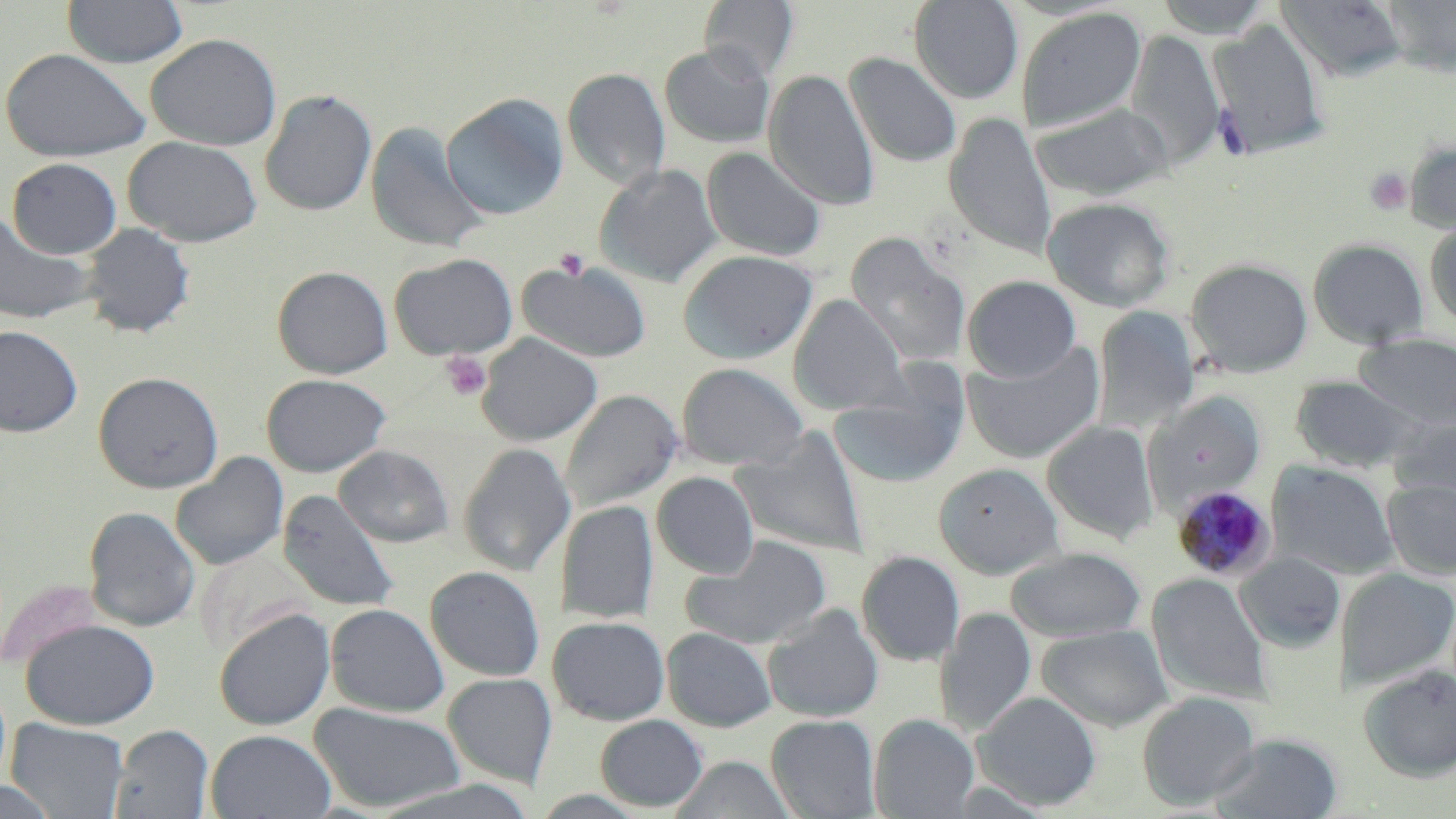
{
  "slide_level_diagnosis": "Plasmodium malariae",
  "modality": "optical microscopy",
  "uninfected_red_blood_cell_locations": "approximate bounding boxes as named x1/y1/x2/y2 corners in pixels: (x1=62, y1=0, x2=188, y2=68), (x1=699, y1=0, x2=798, y2=82), (x1=909, y1=0, x2=1024, y2=103), (x1=1153, y1=0, x2=1276, y2=38), (x1=1276, y1=0, x2=1408, y2=82), (x1=1380, y1=1, x2=1456, y2=77), (x1=1015, y1=6, x2=1147, y2=134), (x1=1209, y1=18, x2=1330, y2=158), (x1=1125, y1=28, x2=1225, y2=169), (x1=145, y1=33, x2=282, y2=151), (x1=660, y1=44, x2=775, y2=148), (x1=0, y1=47, x2=152, y2=162), (x1=844, y1=52, x2=962, y2=168), (x1=562, y1=68, x2=671, y2=189), (x1=764, y1=69, x2=879, y2=210), (x1=260, y1=89, x2=377, y2=216), (x1=441, y1=93, x2=569, y2=221), (x1=1030, y1=101, x2=1172, y2=201), (x1=945, y1=112, x2=1056, y2=258), (x1=366, y1=120, x2=490, y2=253), (x1=123, y1=136, x2=263, y2=247), (x1=1405, y1=140, x2=1456, y2=233), (x1=702, y1=147, x2=827, y2=262), (x1=7, y1=157, x2=122, y2=259), (x1=594, y1=164, x2=722, y2=287), (x1=1042, y1=197, x2=1175, y2=312), (x1=0, y1=210, x2=97, y2=326), (x1=1424, y1=220, x2=1456, y2=329), (x1=79, y1=222, x2=195, y2=338), (x1=845, y1=231, x2=970, y2=370), (x1=1308, y1=238, x2=1429, y2=349), (x1=678, y1=249, x2=818, y2=364), (x1=388, y1=252, x2=518, y2=360), (x1=1186, y1=258, x2=1313, y2=378), (x1=518, y1=259, x2=652, y2=364), (x1=272, y1=265, x2=393, y2=379), (x1=963, y1=275, x2=1081, y2=381), (x1=789, y1=295, x2=905, y2=415), (x1=1093, y1=306, x2=1201, y2=431), (x1=0, y1=325, x2=83, y2=437), (x1=477, y1=333, x2=603, y2=446), (x1=1356, y1=334, x2=1456, y2=429), (x1=963, y1=341, x2=1105, y2=464), (x1=676, y1=362, x2=809, y2=471), (x1=93, y1=371, x2=224, y2=493), (x1=829, y1=371, x2=968, y2=489), (x1=261, y1=373, x2=390, y2=477), (x1=1290, y1=375, x2=1419, y2=473), (x1=560, y1=389, x2=682, y2=514), (x1=1146, y1=390, x2=1265, y2=506), (x1=1388, y1=413, x2=1456, y2=509), (x1=1042, y1=421, x2=1159, y2=545), (x1=731, y1=430, x2=870, y2=557), (x1=459, y1=442, x2=575, y2=577), (x1=335, y1=445, x2=454, y2=547), (x1=171, y1=453, x2=289, y2=571), (x1=1268, y1=460, x2=1399, y2=580), (x1=934, y1=463, x2=1065, y2=579), (x1=652, y1=472, x2=759, y2=578), (x1=1382, y1=479, x2=1456, y2=579), (x1=278, y1=490, x2=401, y2=613), (x1=558, y1=500, x2=658, y2=623), (x1=83, y1=506, x2=200, y2=632), (x1=680, y1=536, x2=832, y2=649), (x1=196, y1=546, x2=313, y2=658), (x1=1006, y1=546, x2=1146, y2=642), (x1=857, y1=551, x2=965, y2=666), (x1=1235, y1=552, x2=1345, y2=652), (x1=425, y1=566, x2=546, y2=682), (x1=1336, y1=568, x2=1456, y2=690), (x1=1148, y1=573, x2=1270, y2=703), (x1=325, y1=603, x2=449, y2=717), (x1=762, y1=604, x2=884, y2=723), (x1=936, y1=607, x2=1037, y2=738), (x1=213, y1=608, x2=335, y2=730), (x1=548, y1=616, x2=669, y2=725), (x1=21, y1=618, x2=160, y2=730), (x1=1036, y1=624, x2=1174, y2=732), (x1=661, y1=627, x2=776, y2=731), (x1=1358, y1=664, x2=1456, y2=781), (x1=442, y1=672, x2=558, y2=787), (x1=974, y1=690, x2=1101, y2=811), (x1=1137, y1=691, x2=1260, y2=809), (x1=309, y1=702, x2=464, y2=813), (x1=595, y1=713, x2=708, y2=812), (x1=766, y1=714, x2=880, y2=818), (x1=869, y1=714, x2=978, y2=818), (x1=5, y1=718, x2=129, y2=819), (x1=110, y1=724, x2=215, y2=819), (x1=206, y1=729, x2=336, y2=819), (x1=1211, y1=732, x2=1342, y2=819), (x1=670, y1=755, x2=796, y2=818), (x1=0, y1=778, x2=60, y2=819)",
  "image_size": "1456×819 pixels",
  "magnification": "1000x",
  "field_of_view": "single",
  "plasmodium_malariae_infected_red_blood_cell_locations": "approximate bounding boxes as named x1/y1/x2/y2 corners in pixels: (x1=1172, y1=485, x2=1277, y2=581)",
  "stain": "May-Grünwald-Giemsa",
  "preparation": "thin blood film",
  "platelet_locations": "approximate bounding boxes as named x1/y1/x2/y2 corners in pixels: (x1=1364, y1=168, x2=1413, y2=216), (x1=555, y1=247, x2=590, y2=280), (x1=441, y1=352, x2=491, y2=401)"
}